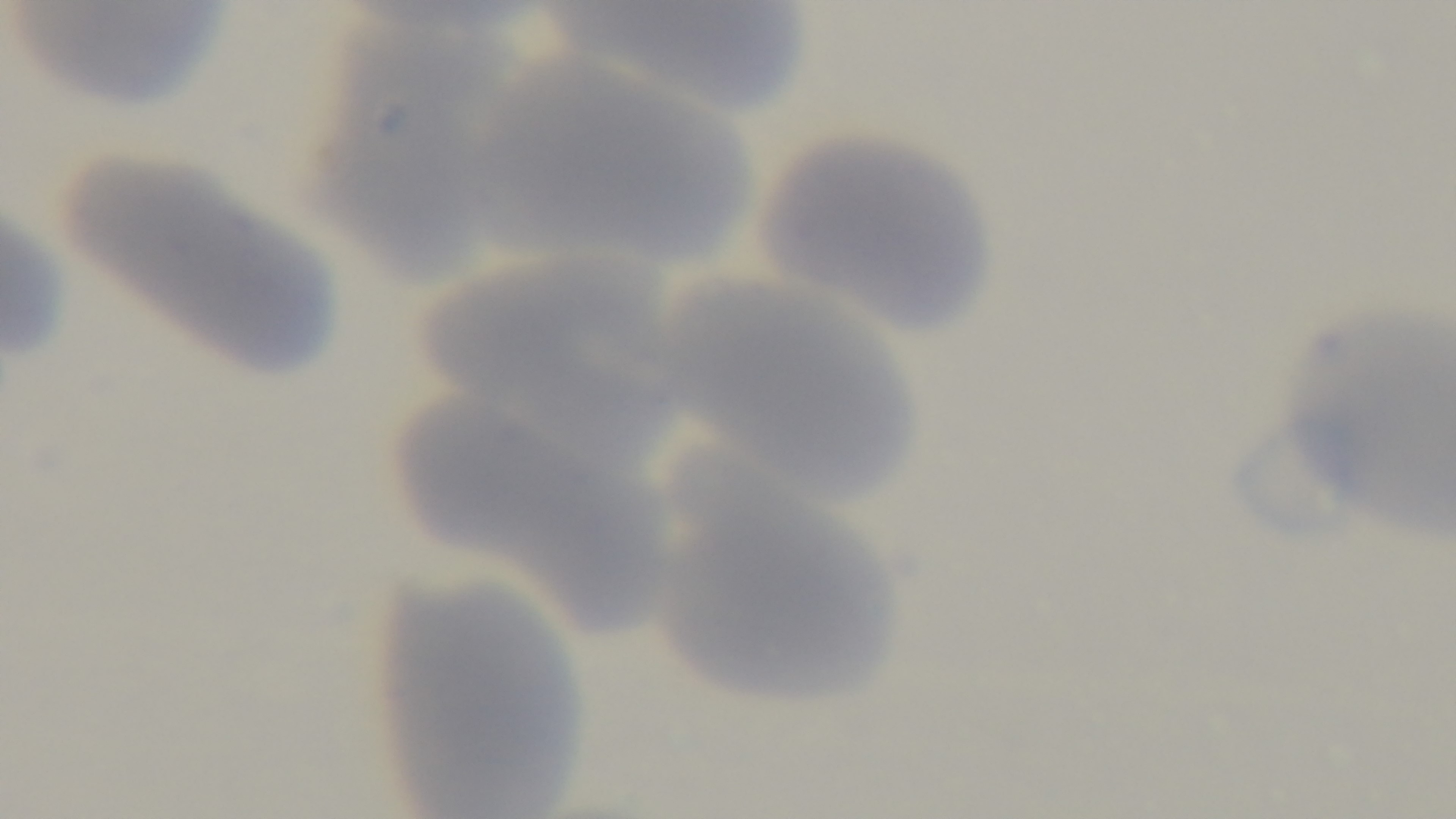
modality = light microscopy
preparation = thin smear
capture = mounted 4K digital camera
malaria status = negative
field of view = single
stain = Giemsa
objective = 100x oil immersion